Identify the cell.
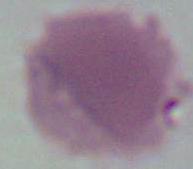

An erythrocyte.

Summary:
  - Modality: photomicrograph
  - Magnification: 1000x